Name the cell type shown.
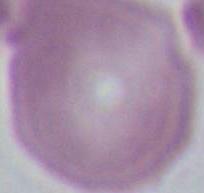

An erythrocyte.

magnification = 1000x
modality = photomicrograph